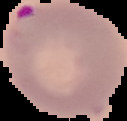

image_size: 127×121 pixels
image_type: segmented cell region on a black background
preparation: thin blood smear
result: Plasmodium parasites identified